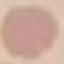
Summary:
  - Result: no malaria parasites seen
  - Capture: smartphone through the microscope eyepiece
  - Preparation: thin blood film
  - Image type: cell patch, automatically extracted from a larger field of view and resized to 64 × 64 pixels
  - Stain: Giemsa